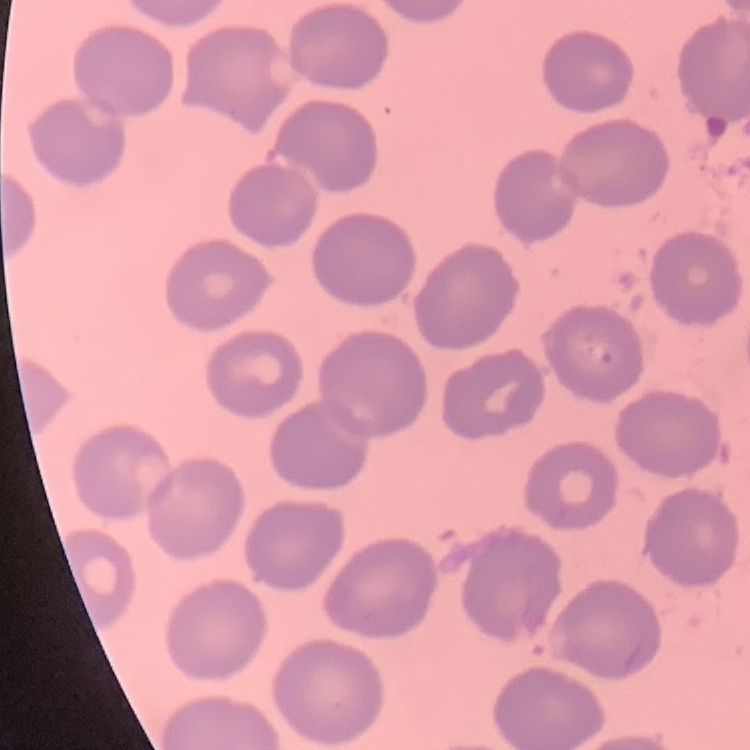

Summary:
  - Erythrocyte morphology: no rouleaux formation
  - Preparation: thin blood film
  - Image type: one tile cut from a larger photomicrograph
  - Stain: Field's or Giemsa